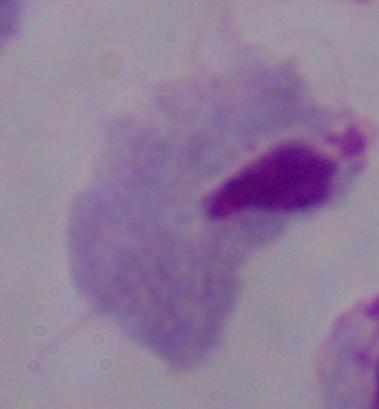

Summary:
  - Identification: trichomonad
  - Modality: photomicrograph
  - Magnification: 1000x